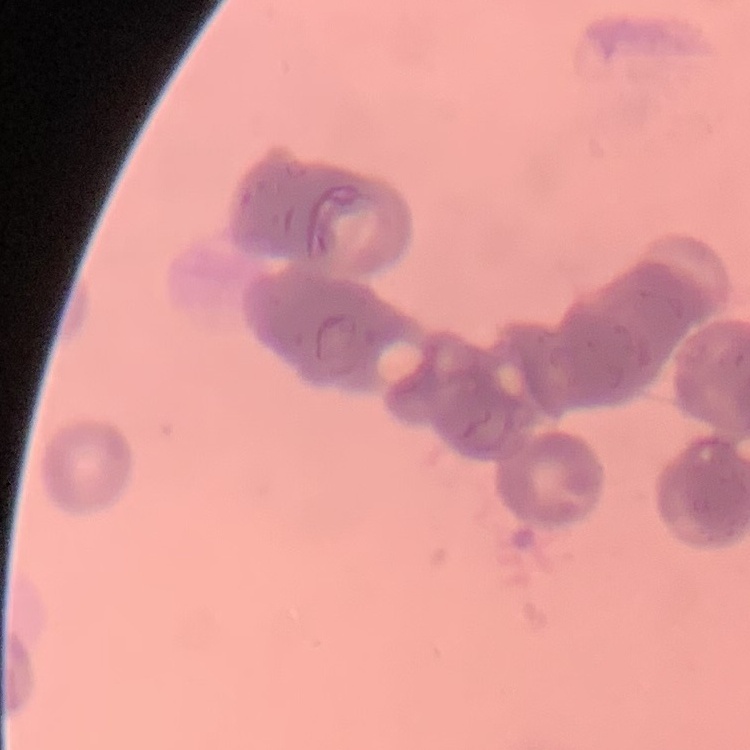
red blood cell morphology = rouleaux formation
preparation = thin blood film
stain = Field's or Giemsa
image type = one tile cut from a larger photomicrograph